Identify the cell.
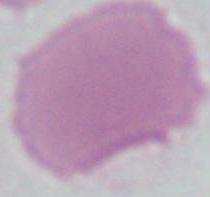
This is an erythrocyte.

Summary:
  - Magnification: 1000x
  - Modality: photomicrograph